Find the cells and give the type of each one.
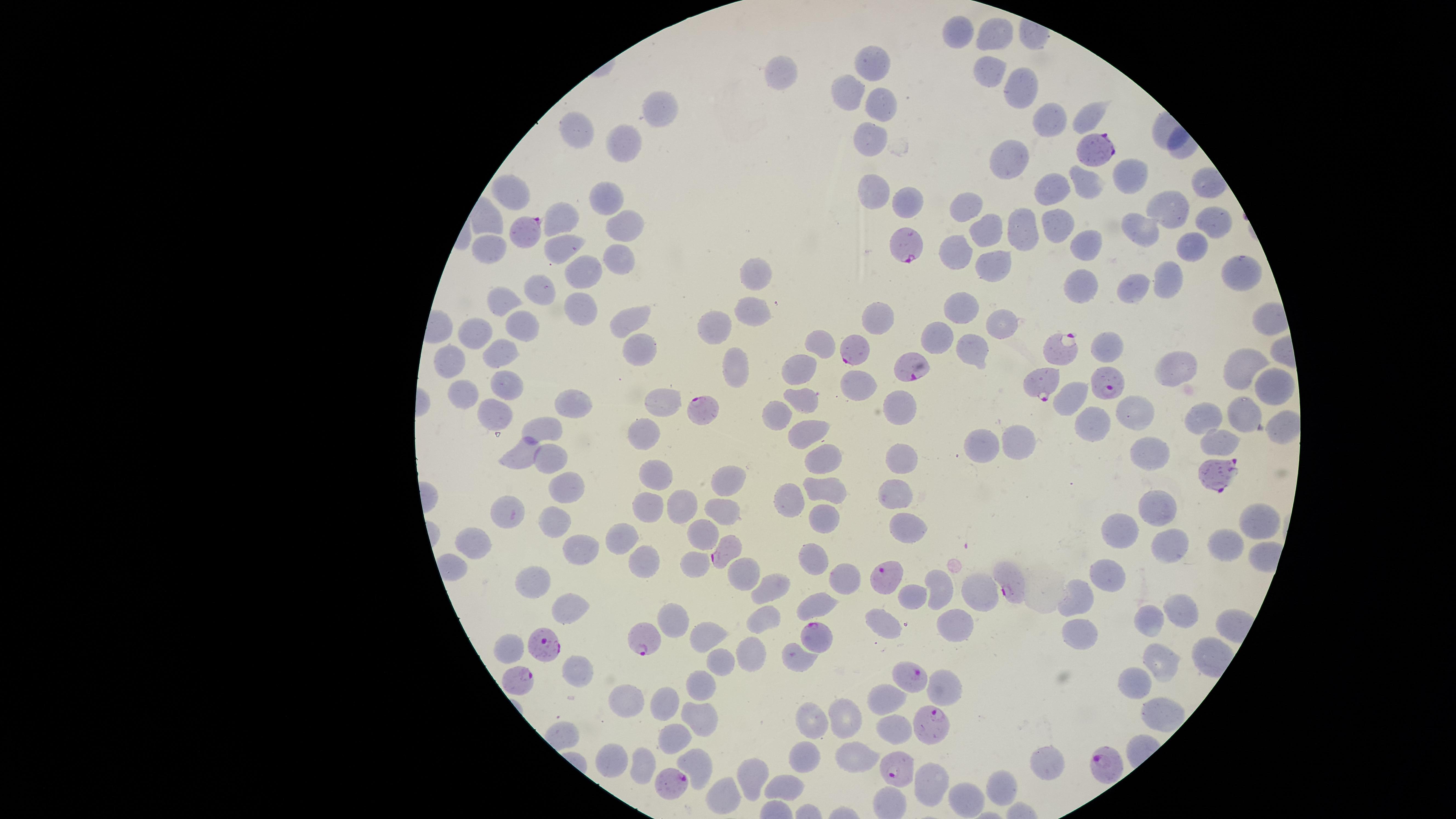

Approximate marker points, in pixels from the top-left corner.
Parasitized red blood cells: (x=1089, y=150), (x=525, y=230), (x=912, y=246), (x=1064, y=343), (x=855, y=352), (x=918, y=367), (x=1107, y=380), (x=1042, y=383), (x=706, y=406), (x=1218, y=474), (x=725, y=550), (x=884, y=578), (x=1008, y=578), (x=814, y=633), (x=647, y=638), (x=547, y=641), (x=916, y=676), (x=522, y=681), (x=927, y=723), (x=1108, y=764), (x=896, y=769), (x=671, y=781).
Uninfected red blood cells: (x=961, y=32), (x=991, y=35), (x=875, y=61), (x=783, y=70), (x=988, y=70), (x=1019, y=87), (x=852, y=89), (x=880, y=108), (x=663, y=112), (x=1090, y=116), (x=1043, y=118), (x=577, y=125), (x=625, y=143), (x=871, y=144), (x=1016, y=162), (x=1130, y=175), (x=1089, y=183), (x=872, y=187), (x=1054, y=188), (x=512, y=193), (x=609, y=197), (x=1170, y=202), (x=911, y=205), (x=973, y=205), (x=563, y=217), (x=1058, y=219), (x=623, y=222), (x=1209, y=224), (x=1142, y=225), (x=990, y=229), (x=1023, y=229), (x=1092, y=240), (x=566, y=244), (x=486, y=249), (x=1188, y=249), (x=959, y=251), (x=620, y=261), (x=989, y=266), (x=757, y=271), (x=588, y=276), (x=1230, y=276), (x=1169, y=279), (x=1078, y=284), (x=1135, y=285), (x=536, y=290), (x=501, y=300), (x=955, y=307), (x=579, y=309), (x=754, y=312), (x=880, y=314), (x=630, y=319), (x=1000, y=323), (x=717, y=328), (x=480, y=331), (x=523, y=332), (x=940, y=335), (x=824, y=338), (x=1112, y=345), (x=635, y=348), (x=501, y=350), (x=974, y=351), (x=452, y=358), (x=734, y=361), (x=1237, y=368), (x=1181, y=369), (x=798, y=375), (x=865, y=385), (x=509, y=387), (x=1262, y=388), (x=464, y=395), (x=1070, y=399), (x=568, y=401), (x=665, y=402), (x=799, y=402), (x=896, y=406), (x=774, y=411), (x=1242, y=411), (x=494, y=412), (x=1133, y=416), (x=1206, y=421), (x=1091, y=422), (x=547, y=426), (x=812, y=430), (x=647, y=431), (x=1217, y=437), (x=1018, y=438), (x=985, y=442), (x=520, y=449), (x=1148, y=451), (x=904, y=454), (x=553, y=457), (x=829, y=460), (x=660, y=471), (x=731, y=475), (x=825, y=487), (x=892, y=489), (x=569, y=490), (x=792, y=494), (x=649, y=503), (x=684, y=503), (x=1161, y=507), (x=505, y=511), (x=722, y=514), (x=823, y=518), (x=554, y=520), (x=1259, y=520), (x=909, y=526), (x=1123, y=526), (x=701, y=531), (x=623, y=534), (x=1231, y=541), (x=1170, y=545), (x=483, y=546), (x=578, y=547), (x=814, y=553), (x=695, y=561), (x=642, y=563), (x=749, y=569), (x=1101, y=571), (x=847, y=578), (x=768, y=579), (x=539, y=582), (x=941, y=587), (x=980, y=593), (x=912, y=596), (x=1079, y=599), (x=818, y=601), (x=569, y=603), (x=1183, y=606), (x=761, y=612), (x=676, y=619), (x=1150, y=626), (x=885, y=627), (x=1074, y=627), (x=949, y=629), (x=704, y=634), (x=509, y=647), (x=750, y=648), (x=792, y=654), (x=723, y=662), (x=1159, y=664), (x=580, y=675), (x=699, y=683), (x=1131, y=687), (x=946, y=690), (x=885, y=695), (x=664, y=702), (x=628, y=703), (x=1158, y=711), (x=842, y=717), (x=697, y=719), (x=810, y=721), (x=896, y=728), (x=672, y=737), (x=854, y=758), (x=1052, y=759), (x=802, y=760), (x=612, y=761), (x=699, y=762), (x=643, y=767), (x=751, y=771), (x=784, y=783), (x=930, y=786), (x=996, y=787), (x=728, y=792), (x=961, y=799).
No white blood cells identified.

field of view = single
stain = Giemsa
visible region = circular
species = Plasmodium falciparum
capture = smartphone photograph through the microscope eyepiece
preparation = thin blood film
image size = 1456×819 pixels